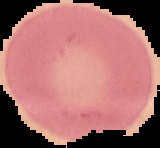 From a thin blood smear. Image is 160×148 pixels. Result: negative for Plasmodium parasites. Cell region segmented out of the field of view; the surrounding area is masked to black.